Identify the parasite.
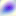

Toxoplasma gondii.

400x magnification. Photomicrograph.